Classify this cell by malaria status.
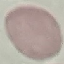

It is uninfected.

Summary:
  - Stain: Giemsa
  - Capture: smartphone through the microscope eyepiece
  - Image type: cell patch, automatically extracted from a larger field of view and resized to 64 × 64 pixels
  - Preparation: thin blood film